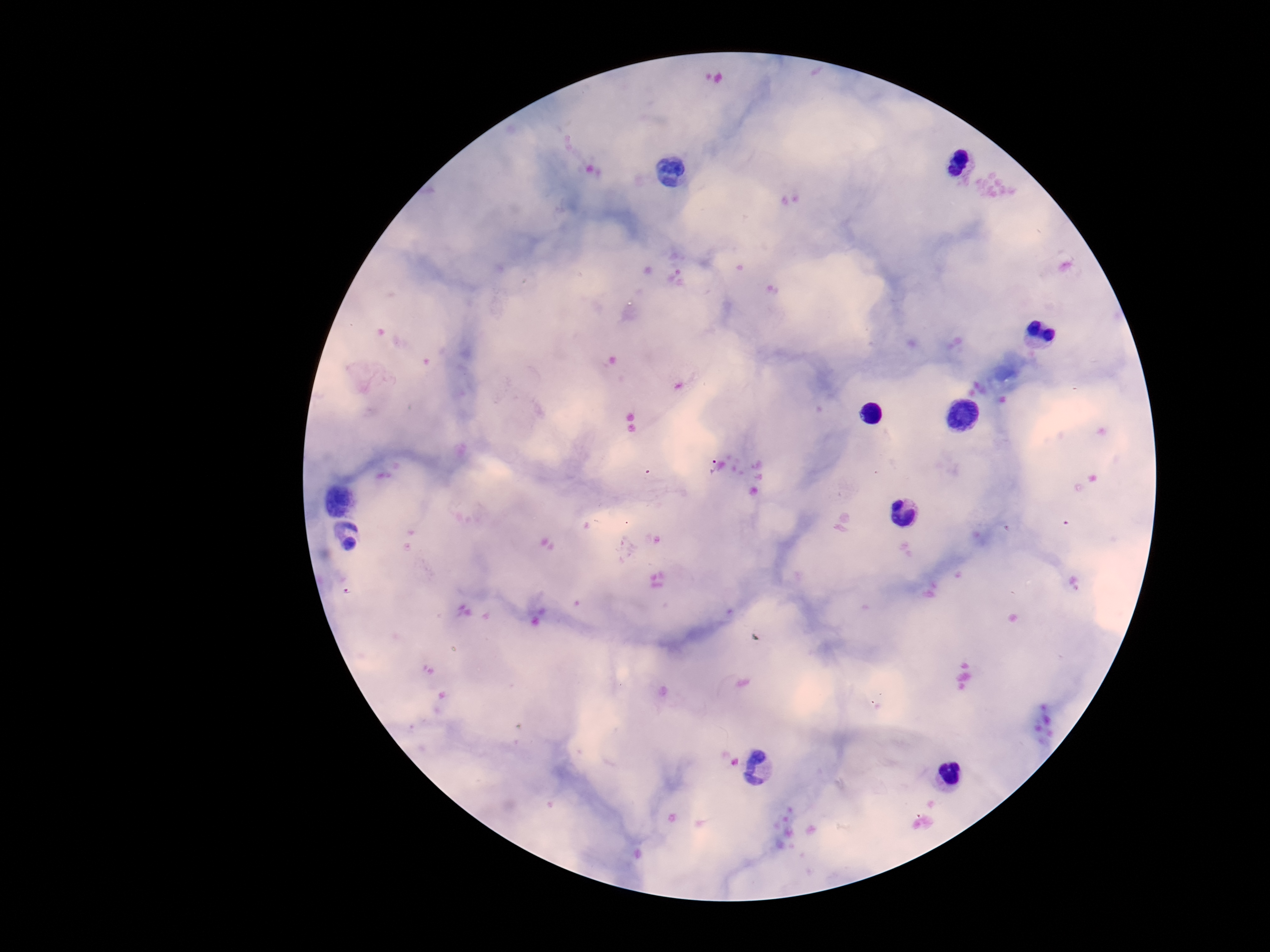
Approximate centers as [x, y] in pixels. Plasmodium parasite locations: [714, 466]. Giemsa stain. Patient malaria status: positive. One field from this slide. Thick blood smear. Smartphone photograph taken through the microscope eyepiece. Image is 1270×952 pixels. 100x magnification.